Assess this cell for malaria.
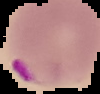

Parasitized.

Summary:
  - Image size: 100×94 pixels
  - Image type: segmented cell region on a black background
  - Preparation: thin blood film